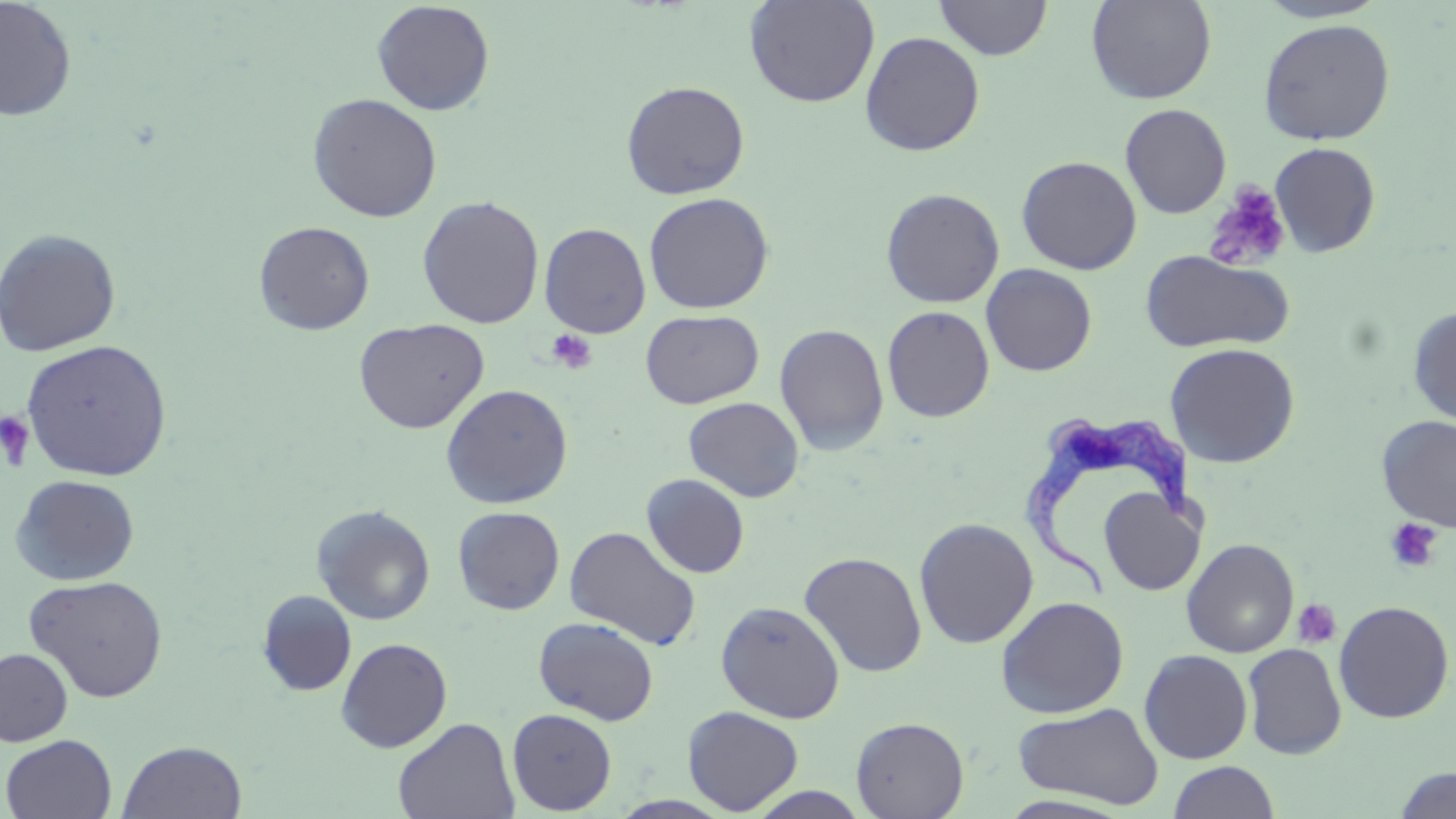
Approximate bounding boxes as (x1, y1, x2, y2) in pixels. Platelet locations: (1204, 183, 1292, 272), (547, 329, 597, 373), (0, 410, 36, 472), (1384, 518, 1442, 573), (1292, 599, 1342, 649). Uninfected red blood cell locations: (0, 0, 77, 122), (744, 0, 880, 108), (934, 0, 1051, 60), (1087, 0, 1217, 104), (1254, 0, 1389, 23), (371, 1, 495, 116), (1257, 19, 1395, 145), (860, 31, 985, 157), (621, 79, 751, 200), (307, 92, 443, 222), (1119, 103, 1232, 218), (1269, 141, 1381, 257), (1016, 155, 1142, 275), (880, 187, 1005, 308), (643, 192, 774, 314), (417, 195, 544, 329), (253, 220, 375, 335), (539, 222, 651, 338), (0, 227, 122, 357), (1140, 250, 1294, 354), (981, 263, 1097, 376), (882, 305, 995, 422), (1407, 305, 1456, 428), (639, 309, 764, 409), (353, 317, 489, 434), (774, 323, 890, 455), (20, 338, 174, 482), (1165, 342, 1301, 468), (440, 383, 574, 508), (684, 397, 804, 502), (1376, 415, 1456, 532), (641, 473, 750, 578), (11, 474, 140, 586), (1099, 488, 1205, 596), (311, 504, 436, 626), (452, 506, 565, 615), (914, 517, 1039, 649), (564, 526, 702, 650), (1181, 538, 1300, 658), (799, 551, 927, 677), (25, 574, 168, 703), (256, 589, 357, 697), (995, 596, 1129, 718), (715, 600, 845, 723), (1333, 600, 1454, 723), (533, 616, 660, 725), (336, 637, 452, 752), (1242, 643, 1347, 759), (0, 647, 73, 747), (1139, 649, 1253, 764), (1012, 702, 1164, 809), (682, 706, 804, 814), (507, 708, 617, 815), (393, 717, 519, 819), (851, 717, 969, 819), (1, 734, 117, 819), (117, 740, 248, 818), (1167, 761, 1280, 819), (1393, 766, 1455, 818), (746, 787, 871, 818). Trypanosoma brucei locations: (1019, 409, 1191, 601). Slide-level diagnosis: Trypanosoma brucei. One field of a larger specimen. Thin blood smear. 1000x magnification. May-Grünwald-Giemsa-stained preparation. Image is 1456×819 pixels. Optical microscopy.